Give the extent of all Trypanosoma brucei.
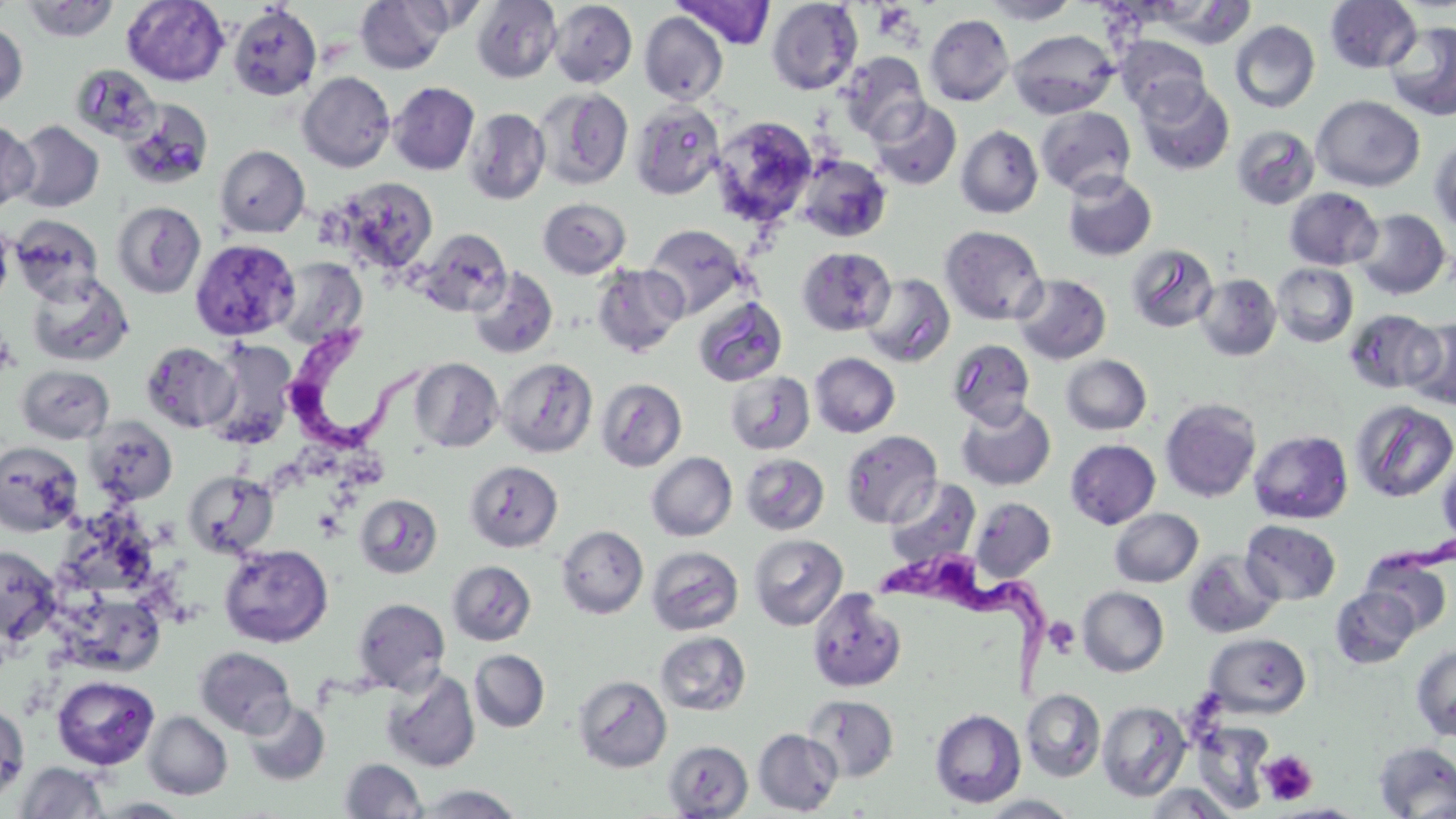

Approximate bounding boxes as [x1, y1, x2, y2] in pixels.
Trypanosoma brucei: [286, 330, 437, 458], [886, 564, 1051, 703].

slide-level diagnosis = Trypanosoma brucei
stain = May-Grünwald-Giemsa
modality = light microscopy
platelet locations = approximate bounding boxes as [x1, y1, x2, y2] in pixels: [1043, 616, 1081, 658], [1259, 750, 1318, 805]
field of view = one of a larger specimen
image size = 1456×819 pixels
preparation = thin blood film
uninfected red blood cell locations = approximate bounding boxes as [x1, y1, x2, y2] in pixels: [122, 0, 229, 86], [355, 0, 452, 74], [472, 0, 562, 83], [981, 0, 1080, 25], [1325, 0, 1422, 73], [20, 1, 120, 42], [549, 1, 637, 88], [672, 1, 776, 49], [767, 1, 863, 95], [228, 4, 321, 100], [639, 12, 728, 105], [924, 13, 1015, 106], [1384, 20, 1456, 122], [1230, 21, 1320, 113], [0, 23, 28, 109], [1009, 29, 1120, 119], [1115, 35, 1210, 119], [838, 51, 929, 142], [71, 64, 161, 145], [297, 71, 395, 172], [1136, 79, 1234, 176], [389, 82, 479, 175], [534, 88, 633, 190], [1312, 96, 1424, 191], [869, 98, 962, 190], [121, 99, 213, 190], [631, 100, 725, 200], [1036, 107, 1136, 197], [465, 108, 550, 205], [711, 115, 818, 227], [0, 119, 39, 211], [10, 120, 104, 213], [955, 125, 1043, 218], [1232, 125, 1319, 209], [1429, 137, 1456, 234], [215, 145, 309, 238], [796, 154, 892, 242], [1061, 171, 1157, 261], [332, 177, 439, 274], [1285, 188, 1382, 270], [538, 198, 631, 278], [112, 201, 206, 298], [1353, 208, 1450, 299], [10, 214, 104, 304], [0, 219, 14, 310], [644, 224, 747, 319], [940, 225, 1048, 325], [417, 228, 511, 317], [190, 238, 300, 340], [1127, 244, 1218, 333], [797, 247, 896, 336], [276, 257, 368, 349], [592, 263, 688, 357], [1272, 263, 1358, 347], [468, 267, 557, 360], [26, 272, 133, 367], [861, 272, 955, 367], [1012, 273, 1111, 365], [1195, 273, 1281, 361], [693, 296, 787, 387], [1344, 309, 1441, 394], [1402, 317, 1456, 410], [204, 339, 299, 447], [947, 339, 1035, 428], [141, 341, 239, 433], [809, 352, 900, 437], [1060, 355, 1152, 435], [410, 358, 503, 453], [498, 358, 598, 458], [17, 365, 114, 443], [724, 370, 815, 455], [596, 378, 687, 471], [1160, 398, 1261, 502], [956, 400, 1056, 491], [1352, 400, 1456, 503], [87, 418, 178, 506], [841, 430, 942, 528], [1249, 430, 1352, 524], [1065, 439, 1160, 529], [0, 441, 83, 537], [646, 452, 737, 541], [740, 453, 829, 535], [1437, 455, 1456, 549], [465, 459, 563, 552], [183, 469, 278, 559], [884, 478, 980, 569], [354, 494, 442, 579], [970, 497, 1056, 583], [1110, 508, 1203, 587], [63, 511, 165, 588], [1240, 520, 1341, 606], [556, 525, 648, 618], [748, 533, 848, 631], [219, 544, 333, 647], [0, 545, 62, 646], [647, 546, 744, 635], [1183, 551, 1282, 638], [1362, 551, 1452, 635], [447, 560, 536, 646], [1077, 586, 1169, 677], [1331, 586, 1419, 669], [807, 588, 907, 694], [60, 597, 166, 680], [352, 598, 450, 694], [655, 632, 751, 716], [1207, 633, 1310, 718], [1411, 644, 1456, 741], [195, 647, 295, 737], [469, 650, 549, 732], [380, 668, 480, 773], [52, 675, 159, 770], [573, 675, 672, 772], [1022, 689, 1105, 782], [804, 695, 899, 783], [0, 699, 29, 805], [243, 699, 330, 786], [1097, 700, 1191, 800], [929, 708, 1027, 809], [143, 711, 232, 799], [1192, 721, 1275, 812], [753, 729, 842, 815], [663, 740, 753, 818], [1373, 742, 1456, 818], [339, 758, 427, 818], [14, 762, 109, 818], [1143, 783, 1239, 818], [414, 784, 525, 818], [979, 795, 1082, 818], [94, 797, 194, 817], [1275, 803, 1368, 818]
magnification = 1000x